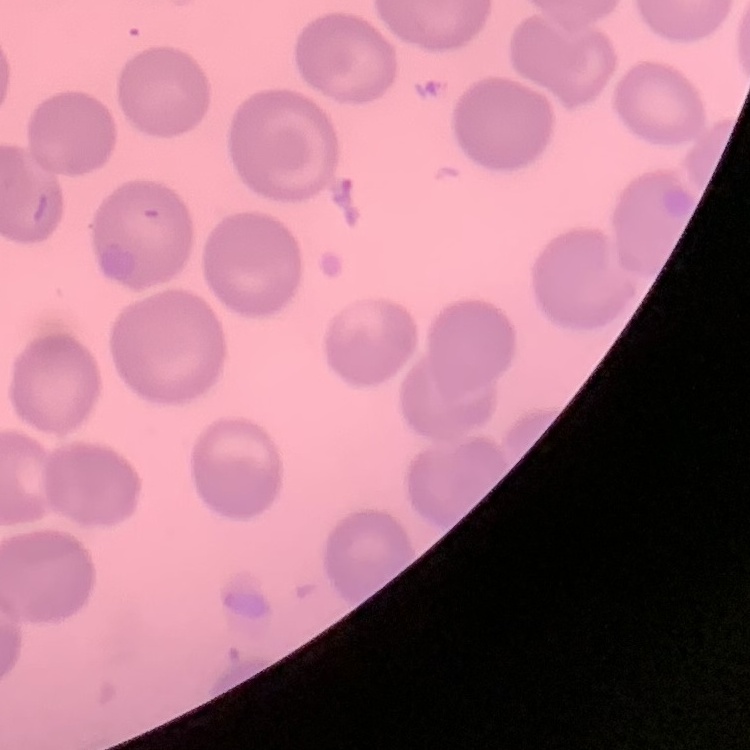 The erythrocytes exhibit no rouleaux formation. Stained with either Field's or Giemsa. Square crop of a larger photomicrograph. Thin peripheral smear.